Identify the parasite.
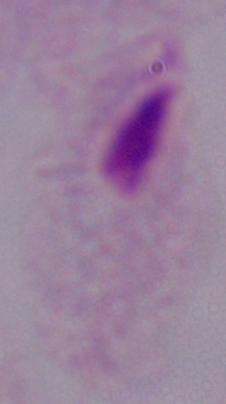

This is a trichomonad.

Summary:
  - Magnification: 1000x
  - Modality: micrograph